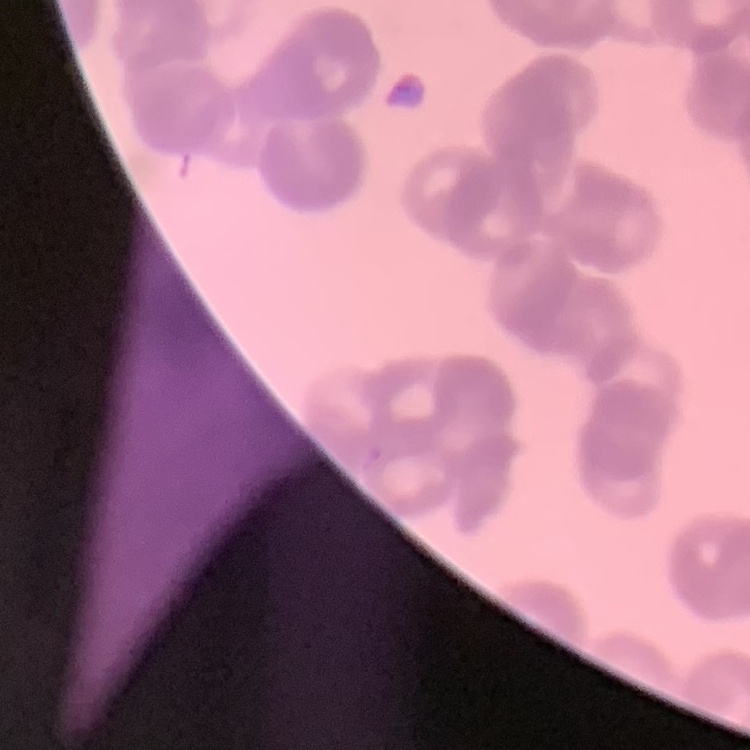
Summary:
  - Red blood cell morphology: rouleaux formation
  - Preparation: thin blood film
  - Image type: square crop of a larger photomicrograph
  - Stain: Field's or Giemsa